Report the malaria status of this cell.
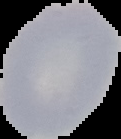

Uninfected.

Image is 121×139 pixels. From a thin blood smear. The area outside the segmented cell region is set to black.